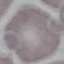

{
  "result": "no malaria parasites detected",
  "image_type": "automatically extracted cell patch, resized to 64 × 64 pixels",
  "capture": "smartphone camera at the microscope eyepiece",
  "preparation": "thin blood film",
  "stain": "Giemsa"
}